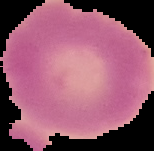

Segmented cell region on a black background. From a thin blood film. Result: no malaria parasites detected. Image is 154×151 pixels.